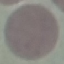

malaria status = uninfected
stain = Giemsa
image type = cell patch, automatically extracted from a larger field of view and resized to 64 × 64 pixels
preparation = thin blood smear
capture = smartphone camera at the microscope eyepiece